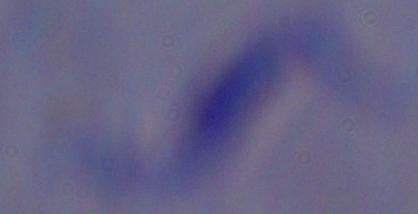

modality = photomicrograph
magnification = 1000x
identification = trypanosome